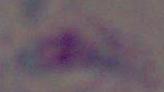 Toxoplasma gondii is seen. Captured at 1000x magnification. Micrograph.